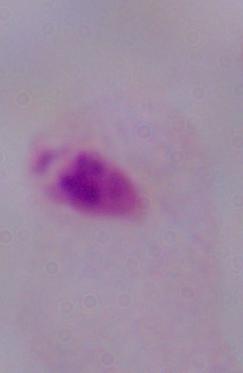 A trichomonad is seen. Micrograph. 1000x magnification.